Point out each leukocyte.
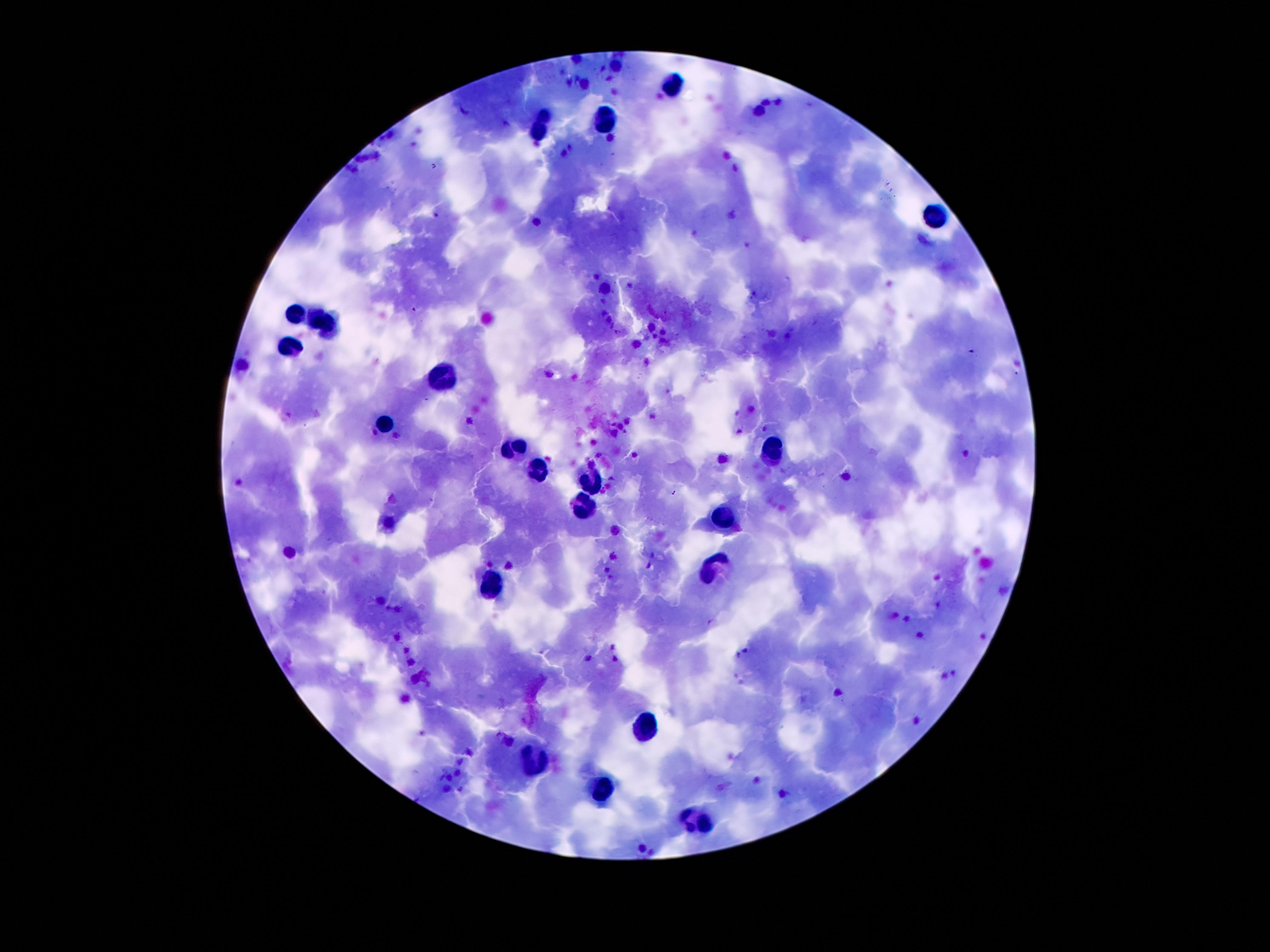

Approximate centers as {x, y} in pixels.
Leukocytes: {676, 90}, {545, 114}, {605, 126}, {540, 133}, {935, 216}, {296, 311}, {314, 315}, {331, 322}, {286, 345}, {245, 364}, {447, 378}, {385, 427}, {523, 444}, {507, 449}, {773, 452}, {540, 469}, {591, 483}, {581, 509}, {731, 519}, {391, 522}, {290, 550}, {715, 568}, {492, 583}, {641, 727}, {529, 763}, {596, 791}, {684, 819}, {703, 821}.

Summary:
  - Plasmodium parasite locations: {766, 430}, {674, 493}
  - Capture: smartphone through the microscope eyepiece
  - Field of view: one from this slide
  - Stain: Giemsa
  - Patient malaria status: positive for Plasmodium falciparum
  - Image size: 1270×952 pixels
  - Preparation: thick peripheral-blood smear
  - Magnification: 100x